Name the cell type shown.
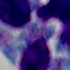
A leukocyte.

magnification = 1000x
modality = photomicrograph